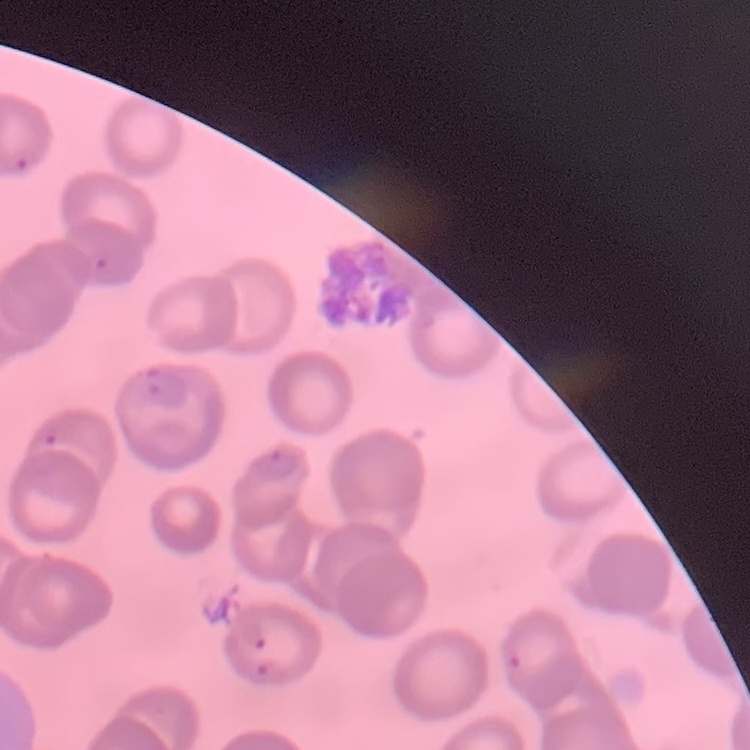 The erythrocytes exhibit no rouleaux formation. Field's or Giemsa stain. Thin peripheral smear. Square crop of a larger photomicrograph.